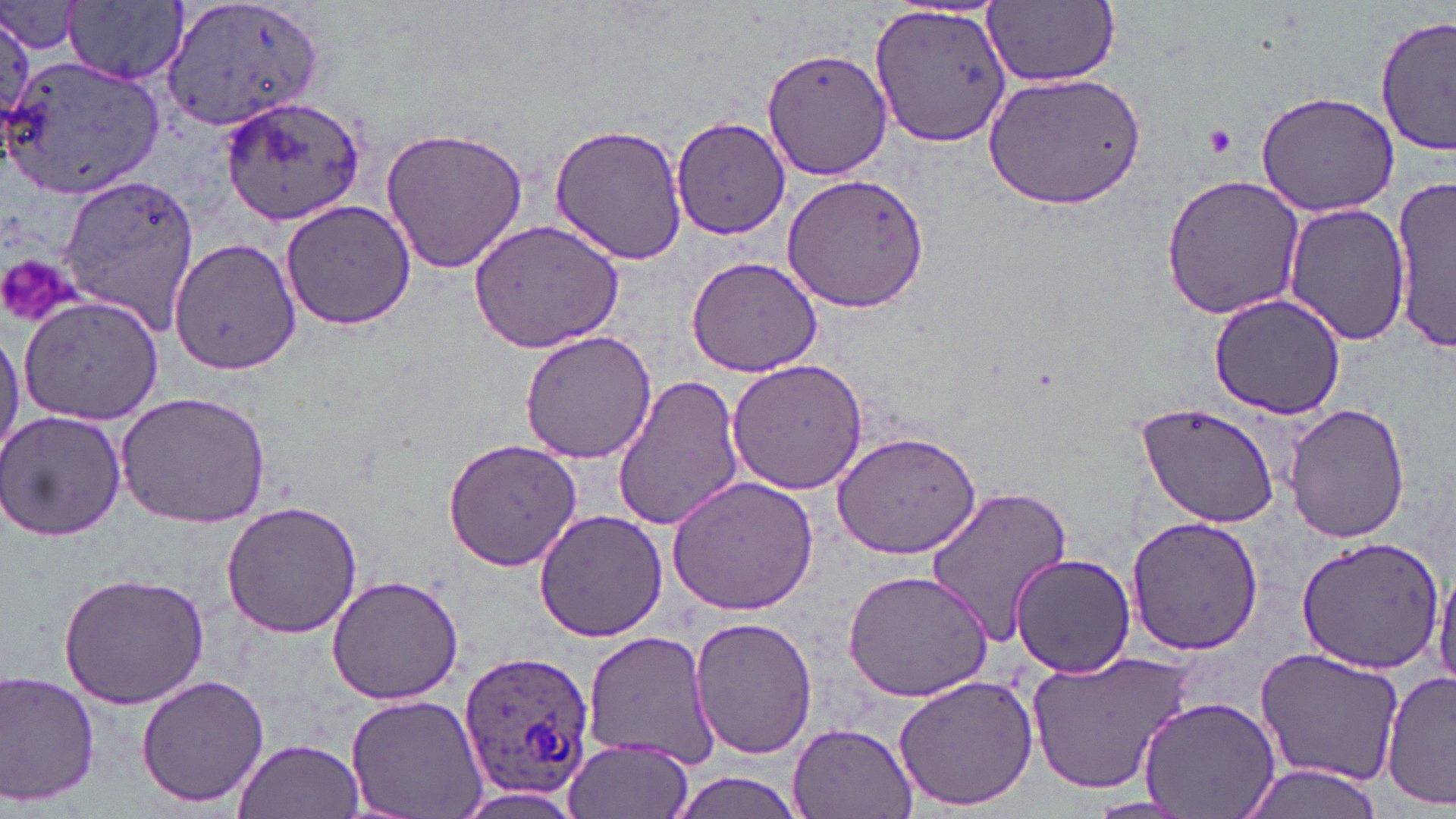

Approximate bounding boxes as (x1,y1)-(x2,y2) corner pairs in pixels. Plasmodium ovale-infected red blood cell locations: (457,647)-(595,804). Platelet locations: (1201,123)-(1239,157), (0,251)-(86,329). Uninfected red blood cell locations: (160,0)-(325,134), (984,1)-(1119,86), (0,2)-(85,57), (67,2)-(188,86), (867,2)-(1014,150), (0,7)-(37,128), (1377,15)-(1455,158), (764,48)-(894,182), (2,51)-(164,200), (984,72)-(1146,211), (1254,90)-(1400,215), (224,93)-(369,226), (676,116)-(794,240), (551,124)-(686,264), (378,126)-(532,274), (783,168)-(930,314), (59,172)-(198,335), (1161,173)-(1305,322), (1391,175)-(1455,349), (280,199)-(415,331), (1282,201)-(1410,348), (467,217)-(625,355), (169,238)-(301,377), (685,252)-(828,377), (1209,294)-(1348,420), (18,295)-(162,426), (0,323)-(23,466), (519,330)-(660,465), (726,357)-(869,494), (610,372)-(749,532), (115,390)-(271,526), (1137,402)-(1283,530), (1284,402)-(1410,546), (1,408)-(126,542), (832,430)-(981,561), (443,438)-(585,573), (666,475)-(819,616), (922,484)-(1074,646), (221,500)-(364,639), (534,508)-(667,643), (1125,515)-(1265,656), (1297,535)-(1446,673), (1010,553)-(1136,678), (1431,562)-(1456,690), (843,567)-(994,702), (58,571)-(210,708), (325,573)-(463,705), (691,615)-(818,761), (582,630)-(720,767), (1255,648)-(1407,785), (1024,651)-(1196,793), (1383,670)-(1456,810), (0,671)-(101,808), (893,674)-(1038,813), (136,675)-(269,810), (345,694)-(486,819), (1137,696)-(1281,819), (789,721)-(919,819), (561,735)-(696,819), (233,738)-(364,819), (1233,764)-(1386,819), (668,771)-(812,819), (1081,798)-(1199,819). Slide-level diagnosis: Plasmodium ovale. Single field of view. Thin blood film. Image is 1456×819 pixels. May-Grünwald-Giemsa-stained preparation. Light microscopy. Captured at 1000x magnification.